Locate every Plasmodium falciparum-infected red blood cell.
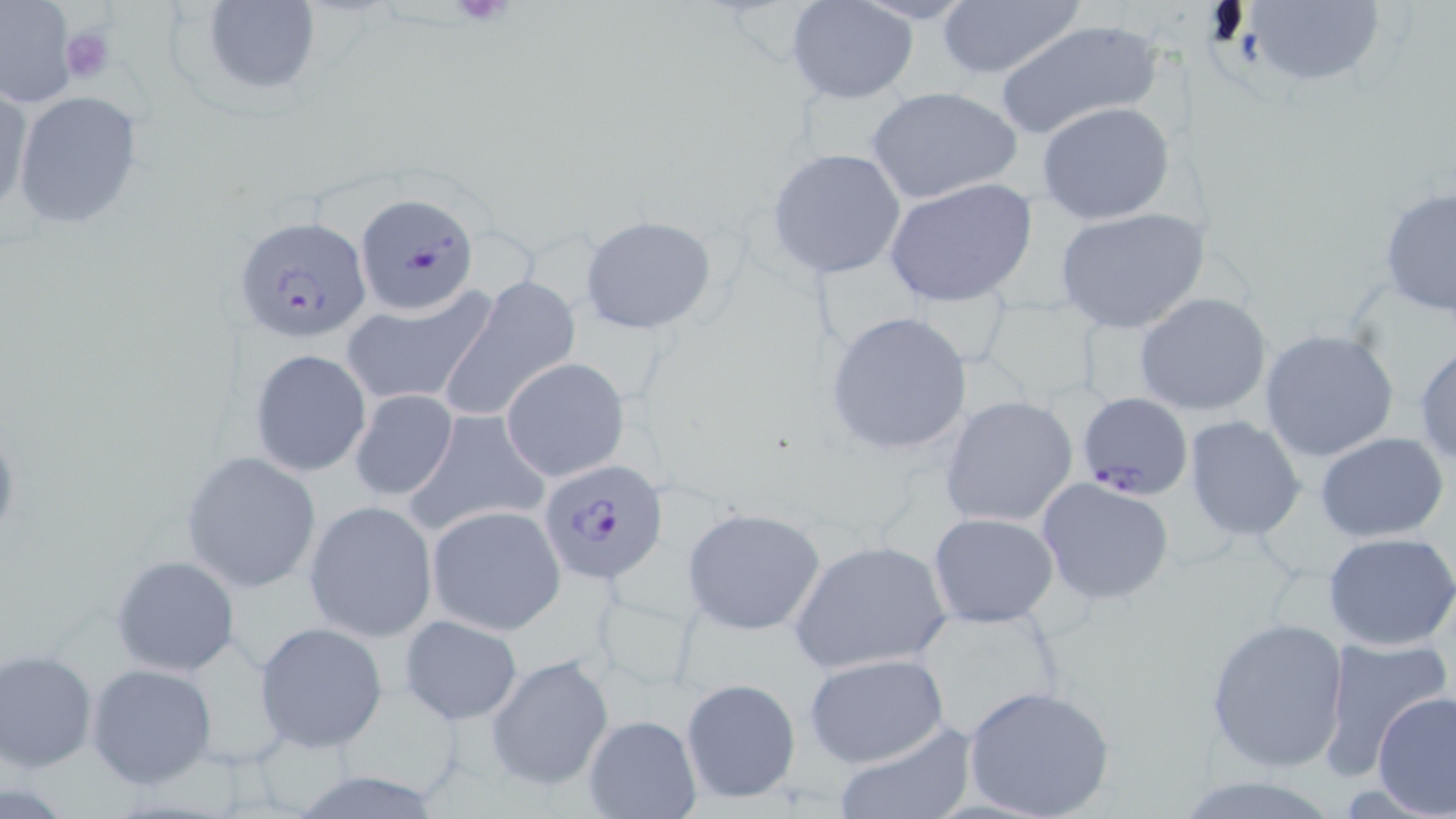

Approximate bounding boxes as (x1,y1)-(x2,y2) corner pairs in pixels.
Plasmodium falciparum-infected red blood cells: (356,192)-(478,317), (235,217)-(372,344), (1078,391)-(1194,499), (537,457)-(669,585).

Uninfected red blood cell locations: (202,0)-(321,96), (934,0)-(1086,83), (1240,0)-(1390,89), (788,1)-(919,104), (0,3)-(79,107), (994,20)-(1166,142), (1,83)-(32,221), (864,85)-(1025,207), (11,90)-(145,231), (1036,101)-(1176,225), (767,148)-(911,280), (884,178)-(1038,306), (1378,187)-(1456,320), (1054,206)-(1210,334), (578,214)-(714,334), (441,277)-(579,422), (340,287)-(497,408), (1134,292)-(1271,417), (823,309)-(974,458), (1259,328)-(1399,463), (1415,343)-(1456,469), (249,347)-(372,477), (502,357)-(631,483), (349,389)-(458,502), (939,394)-(1078,529), (404,409)-(550,538), (1184,416)-(1308,540), (1315,432)-(1452,544), (180,451)-(323,593), (1035,477)-(1176,606), (304,501)-(438,641), (427,505)-(566,636), (681,505)-(826,636), (927,512)-(1060,626), (1322,531)-(1456,651), (788,538)-(954,674), (110,554)-(241,677), (397,614)-(525,725), (1205,614)-(1352,773), (254,621)-(389,753), (1314,637)-(1452,779), (0,648)-(98,772), (803,653)-(951,768), (485,655)-(614,792), (85,662)-(219,790), (680,677)-(801,805), (962,683)-(1117,819), (1371,690)-(1455,815), (585,713)-(700,819), (832,725)-(975,819), (1171,775)-(1345,818). Platelet locations: (450,0)-(519,30), (61,25)-(116,84). Slide-level diagnosis: Plasmodium falciparum. Image is 1456×819 pixels. Captured at 1000x magnification. May-Grünwald-Giemsa stain. Thin blood smear. Optical microscopy. Single field of view.